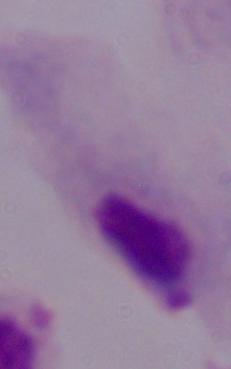

{
  "modality": "micrograph",
  "magnification": "1000x",
  "identification": "trichomonad"
}